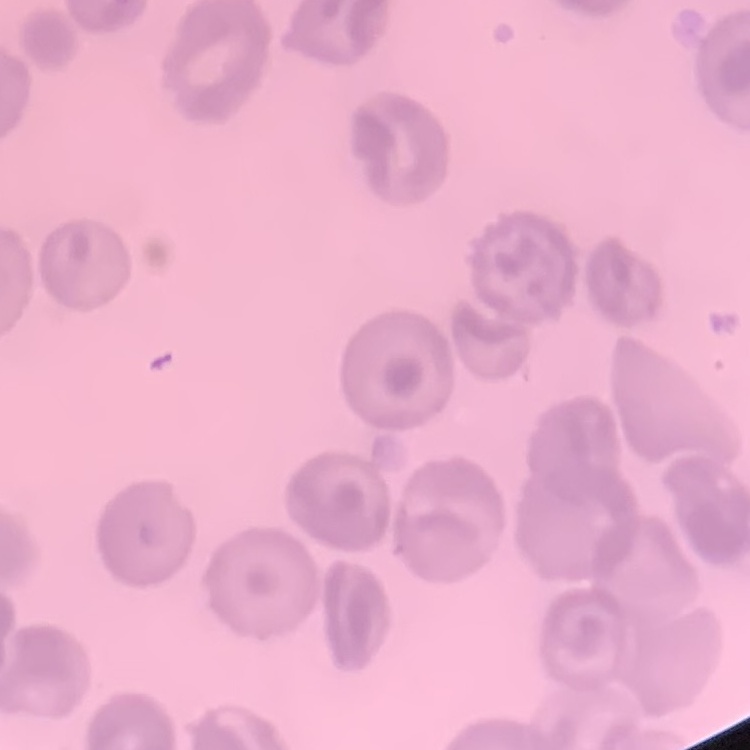
red blood cell morphology = no rouleaux formation
image type = square crop of a larger photomicrograph
stain = Field's or Giemsa
preparation = thin blood smear